State the preparation type.
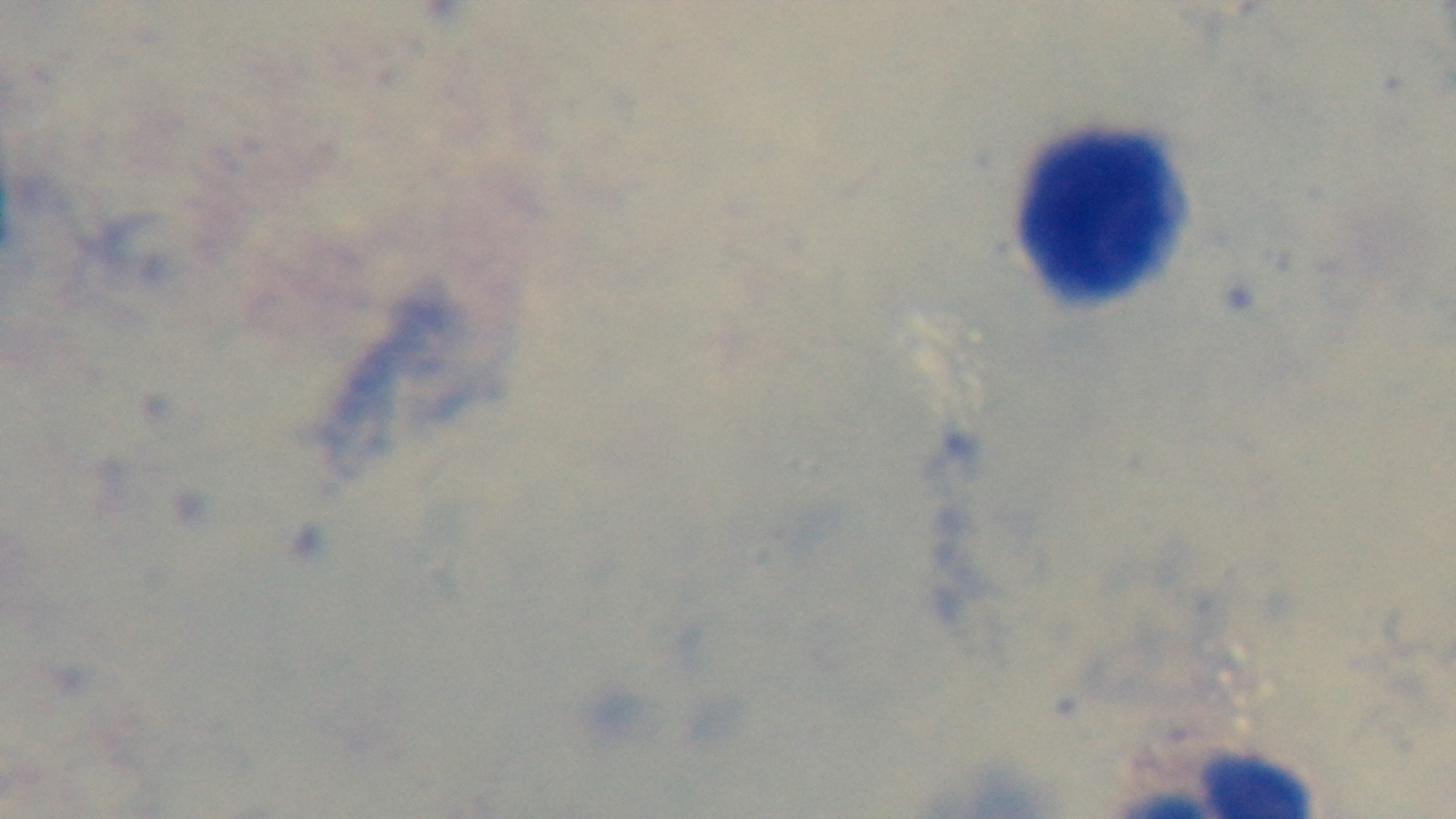

Thick.

Giemsa stain. Photomicrograph. Mounted 4K digital camera. 100x oil-immersion objective. One field from the slide. Malaria status: negative.